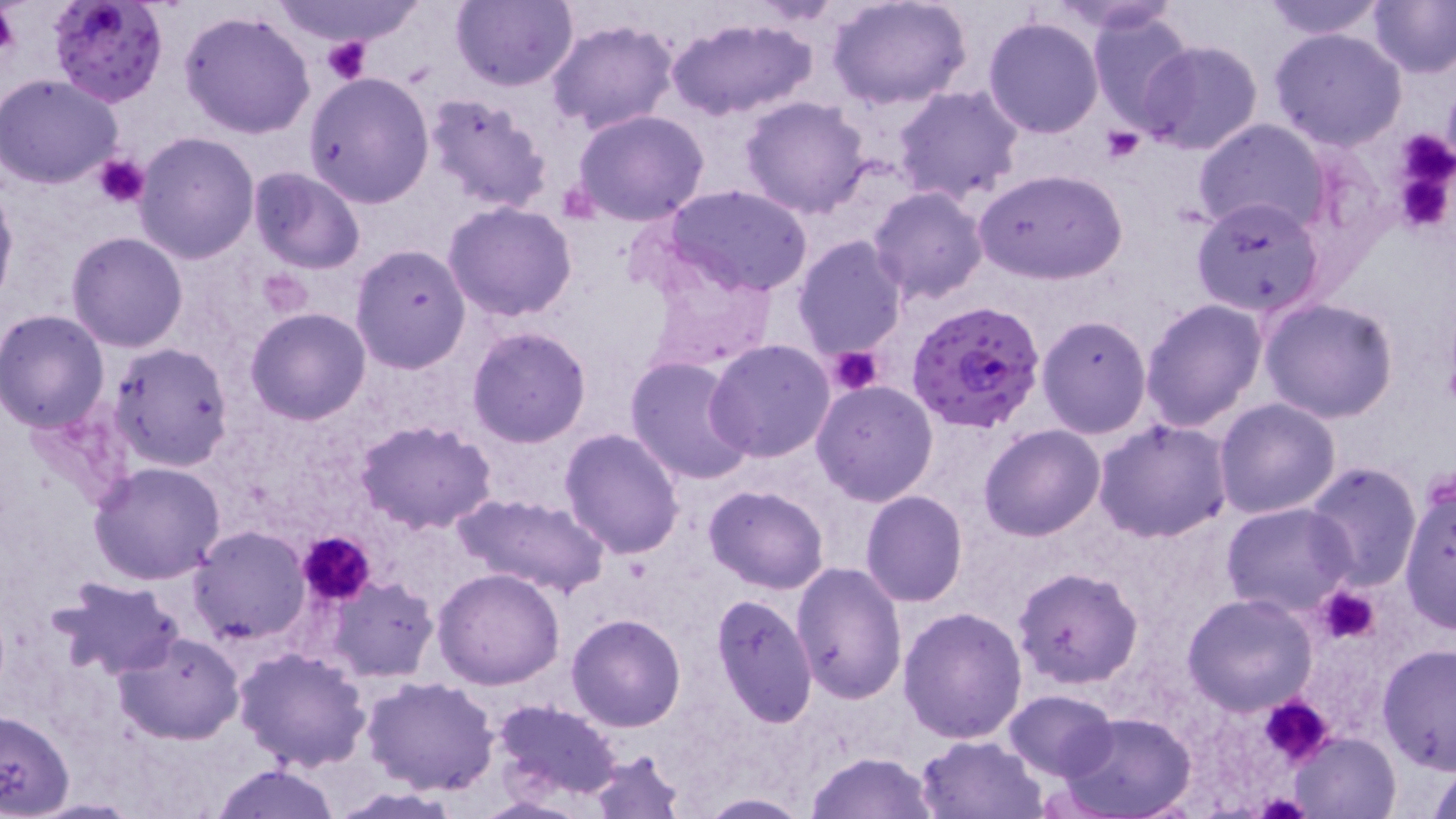

Summary:
  - Coordinate format: approximate bounding boxes as [x1, y1, x2, y2] in pixels
  - Plasmodium falciparum-infected red blood cell locations: [50, 0, 167, 107], [905, 297, 1044, 436]
  - Uninfected red blood cell locations: [268, 0, 423, 47], [453, 0, 579, 92], [827, 0, 971, 110], [1258, 0, 1388, 40], [1367, 0, 1456, 78], [1042, 1, 1184, 33], [1088, 6, 1195, 130], [179, 9, 316, 139], [667, 16, 819, 121], [983, 17, 1104, 138], [544, 19, 679, 134], [1271, 28, 1406, 151], [1137, 39, 1264, 156], [304, 72, 434, 210], [0, 73, 125, 190], [894, 85, 1024, 205], [421, 94, 553, 214], [739, 95, 874, 220], [570, 110, 713, 225], [1193, 118, 1330, 238], [131, 131, 259, 263], [247, 167, 365, 274], [974, 168, 1126, 285], [0, 180, 18, 311], [664, 185, 814, 298], [868, 186, 988, 305], [1190, 196, 1327, 318], [444, 200, 577, 323], [67, 231, 190, 351], [789, 235, 908, 359], [350, 243, 470, 373], [638, 251, 779, 374], [1259, 297, 1398, 424], [1140, 298, 1268, 432], [246, 308, 370, 425], [0, 311, 108, 431], [1036, 314, 1153, 439], [466, 326, 593, 447], [706, 340, 837, 463], [109, 342, 233, 472], [625, 356, 754, 485], [810, 380, 939, 505], [1214, 398, 1341, 518], [1095, 417, 1231, 543], [356, 419, 499, 534], [978, 424, 1105, 541], [559, 427, 686, 557], [1300, 461, 1422, 591], [88, 462, 228, 586], [1398, 480, 1455, 633], [704, 485, 830, 594], [861, 490, 968, 607], [453, 494, 608, 600], [1222, 502, 1356, 619], [188, 526, 309, 646], [791, 562, 907, 704], [1012, 567, 1143, 689], [432, 568, 565, 689], [321, 575, 440, 682], [50, 577, 184, 679], [1181, 592, 1319, 715], [711, 594, 818, 729], [898, 605, 1028, 743], [566, 613, 686, 732], [112, 629, 245, 745], [1376, 643, 1455, 776], [233, 646, 373, 771], [361, 675, 499, 793], [1003, 689, 1118, 780], [489, 699, 624, 804], [0, 706, 74, 817], [1058, 712, 1199, 819], [1290, 733, 1400, 819], [916, 734, 1049, 819], [587, 749, 686, 819], [805, 751, 942, 819], [1426, 759, 1456, 819], [208, 763, 342, 819], [693, 794, 813, 817]
  - Platelet locations: [0, 3, 21, 60], [320, 38, 372, 85], [1101, 127, 1145, 163], [1390, 130, 1456, 233], [93, 154, 150, 208], [828, 345, 886, 396], [295, 532, 377, 606], [1315, 586, 1382, 645], [1259, 696, 1335, 767]
  - Slide-level diagnosis: Plasmodium falciparum
  - Modality: light microscopy
  - Field of view: single
  - Magnification: 1000x
  - Stain: May-Grünwald-Giemsa
  - Image size: 1456×819 pixels
  - Preparation: thin blood film